Locate every malaria parasite and every leukocyte.
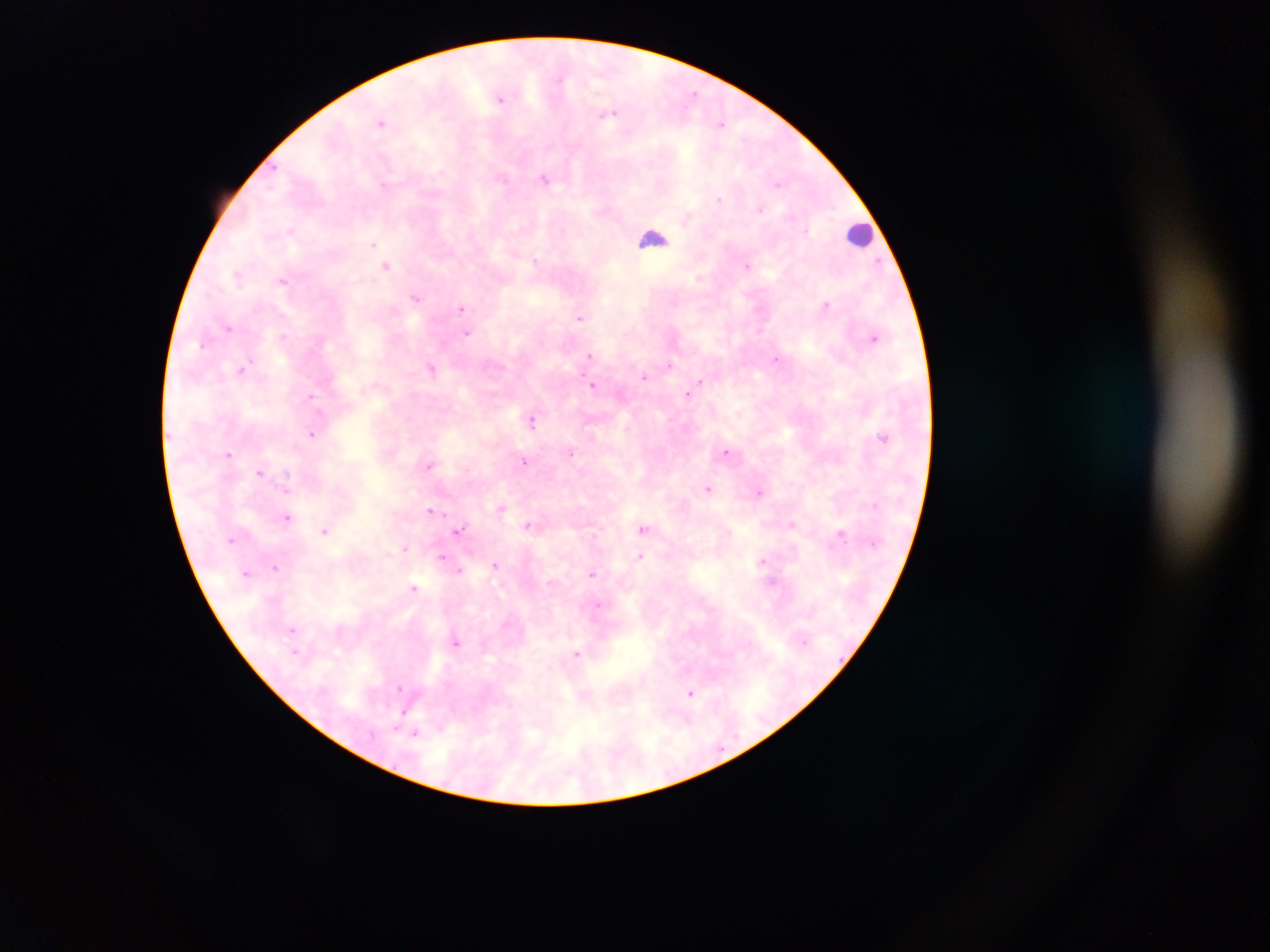
Approximate centers as x y in pixels.
Malaria parasites: 693 93; 500 98; 610 114; 381 123; 721 124; 503 179; 545 179; 778 184; 383 186; 720 199; 760 208; 806 230; 373 244; 534 259; 879 262; 387 265; 747 266; 238 275; 282 281; 416 298; 826 305; 461 308; 579 318; 229 327; 468 333; 283 335; 874 337; 203 344; 588 355; 777 359; 670 365; 431 368; 242 369; 643 377; 700 381; 594 385; 688 395; 311 396; 532 420; 312 433; 726 451; 229 453; 571 453; 525 461; 429 465; 260 472; 286 486; 708 488; 759 494; 501 508; 430 511; 286 518; 792 525; 527 526; 643 528; 459 530; 325 531; 841 534; 405 547; 442 556; 640 557; 762 562; 494 565; 276 567; 459 570; 591 574; 413 587; 598 606; 292 629; 455 642; 295 651; 577 654; 399 688; 691 693; 402 713; 416 733.
Leukocytes: 861 234; 653 238.

Thick blood smear. Collected in Ghana. Photographed through a microscope with a mobile-phone camera. Image is 1270×952 pixels. One field of view.